Outline each blood parasite and name the species.
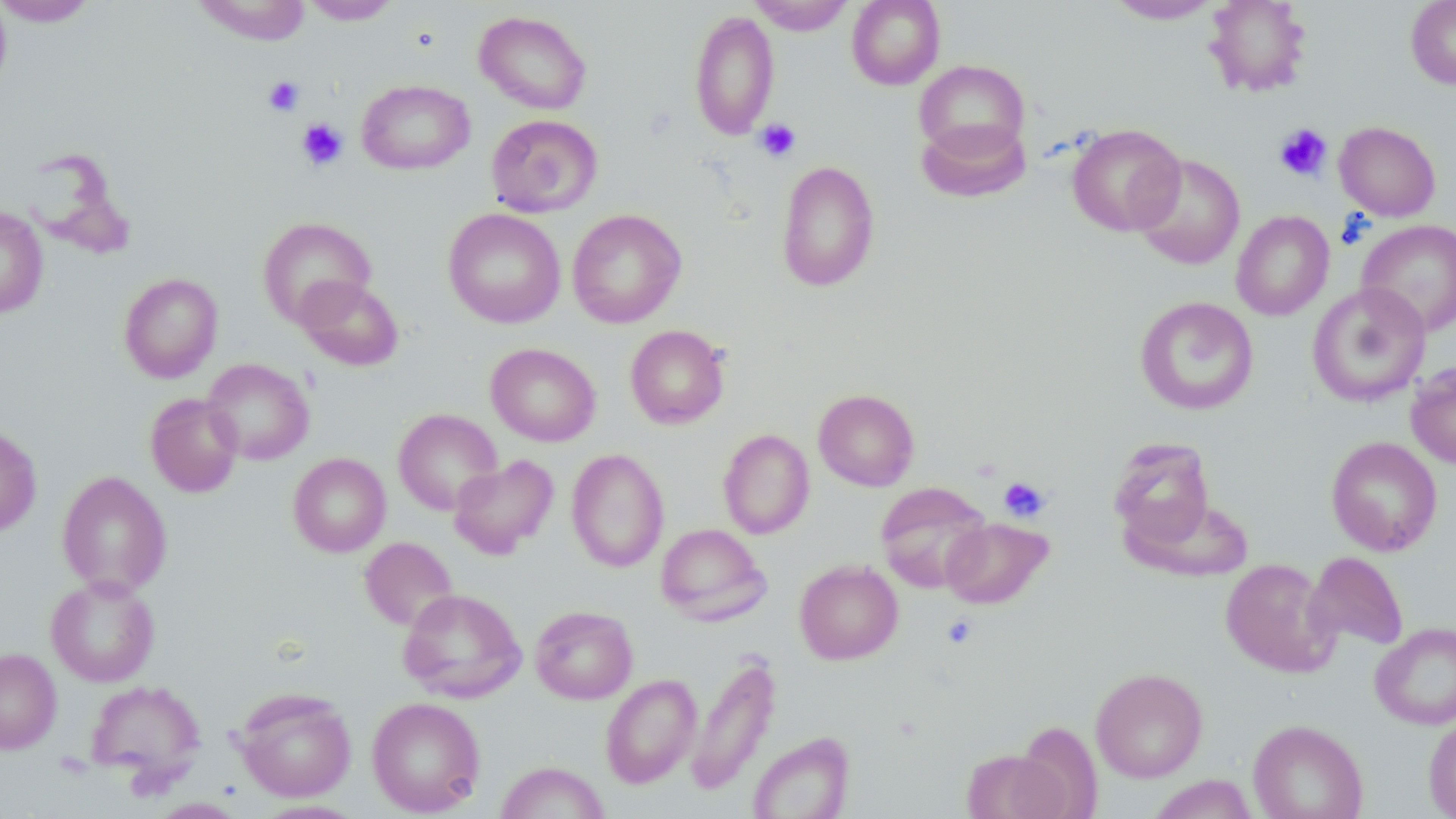
No blood parasites observed.

slide-level diagnosis = negative for blood parasites
magnification = 1000x
field of view = single
stain = May-Grünwald-Giemsa
modality = light microscopy
platelet locations = approximate bounding boxes as (x1,y1)-(x2,y2) corner pairs in pixels: (263,76)-(305,116), (297,118)-(348,170), (755,119)-(801,161), (1273,123)-(1332,181), (998,476)-(1051,523)
uninfected red blood cell locations = approximate bounding boxes as (x1,y1)-(x2,y2) corner pairs in pixels: (0,0)-(99,25), (0,0)-(12,97), (748,0)-(854,35), (847,0)-(945,90), (1105,0)-(1222,23), (1203,0)-(1312,98), (1406,0)-(1456,90), (194,1)-(310,45), (301,1)-(400,25), (474,10)-(592,115), (689,11)-(779,140), (914,60)-(1029,159), (357,80)-(474,174), (486,113)-(603,217), (916,117)-(1031,203), (1334,121)-(1441,221), (1067,123)-(1185,236), (1131,154)-(1245,270), (775,159)-(880,292), (0,206)-(48,318), (443,208)-(565,328), (566,209)-(687,328), (1231,210)-(1334,320), (257,217)-(376,327), (1356,220)-(1456,337), (119,273)-(223,383), (295,275)-(403,371), (1307,283)-(1431,407), (1134,296)-(1259,416), (625,325)-(729,429), (486,343)-(601,446), (202,358)-(315,465), (1406,361)-(1456,469), (813,388)-(920,491), (145,393)-(243,497), (393,408)-(502,515), (0,425)-(42,537), (718,429)-(814,539), (1326,436)-(1442,556), (1108,437)-(1217,550), (566,449)-(669,572), (288,452)-(390,557), (449,454)-(558,560), (57,470)-(171,596), (875,482)-(991,592), (941,517)-(1052,609), (656,523)-(770,625), (360,536)-(458,631), (1304,551)-(1408,653), (1221,558)-(1338,677), (794,560)-(903,664), (45,575)-(160,687), (398,588)-(526,702), (530,605)-(638,704), (1370,622)-(1456,729), (0,648)-(61,754), (685,655)-(780,795), (1090,667)-(1208,782), (601,674)-(701,788), (85,679)-(206,784), (236,688)-(356,801), (366,697)-(486,816), (1423,713)-(1456,818), (1248,719)-(1367,819), (748,731)-(854,819), (962,748)-(1070,819), (495,761)-(610,819), (1146,775)-(1259,819), (149,798)-(247,818), (253,800)-(367,818)
image size = 1456×819 pixels
preparation = thin blood smear